Comment on the morphology of the erythrocytes.
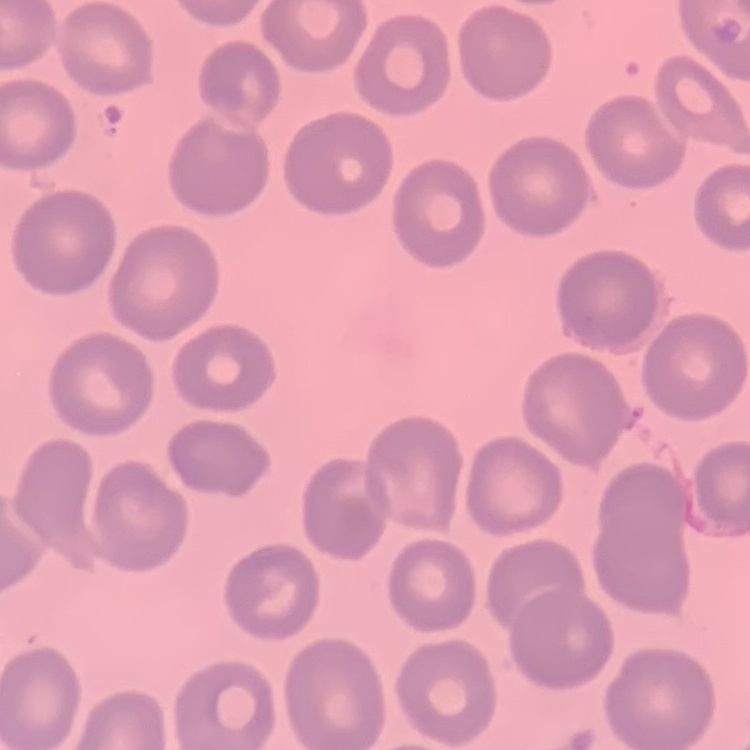

They show no rouleaux formation.

Stained with either Field's or Giemsa. Square crop of a larger photomicrograph. Thin blood smear.